Identify the preparation type.
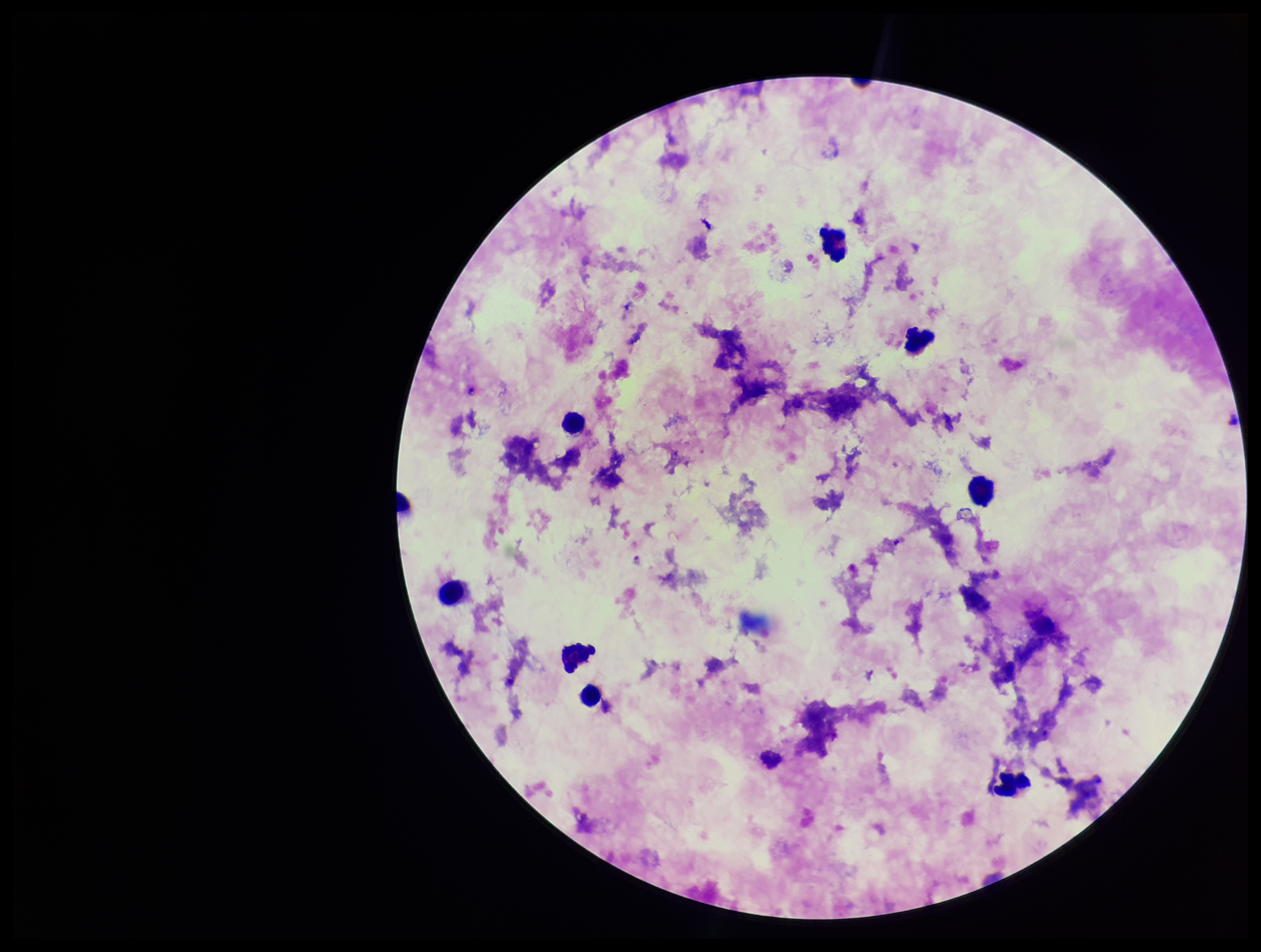
A thick smear.

Smartphone photograph taken through the eyepiece of a microscope. Giemsa stain. Patient malaria status: positive. Plasmodium parasites: detected. One field from this slide. Species reported for this patient: Plasmodium falciparum. Leukocyte count: 8. Image is 1261×952 pixels. Parasite count: 1.